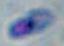

Toxoplasma gondii is shown. 1000x magnification. Photomicrograph.